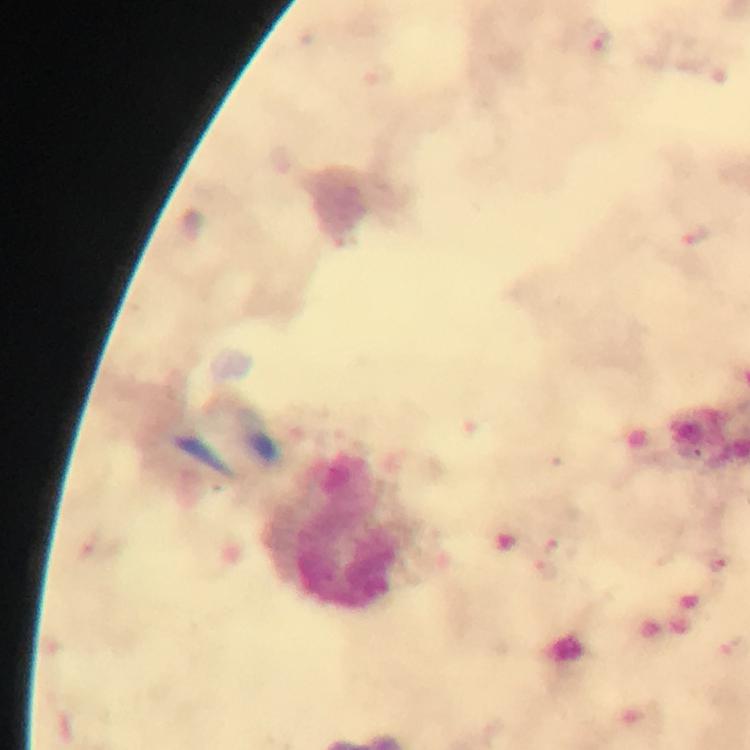

{
  "stain": "Giemsa",
  "context": "from a diagnostic examination for malaria",
  "cropped_from": "a single field of view",
  "preparation": "thick smear",
  "capture": "smartphone camera through the microscope",
  "magnification": "100x",
  "malaria_parasite_locations": "approximate centers as [x, y] in pixels: [598, 36], [694, 237], [720, 564]",
  "image_size": "750×750 pixels",
  "immersion_oil": "applied"
}